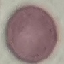
result = no malaria parasites detected
preparation = thin blood smear
stain = Giemsa
image type = automatically extracted cell patch, resized to 64 × 64 pixels
capture = smartphone camera at the microscope eyepiece